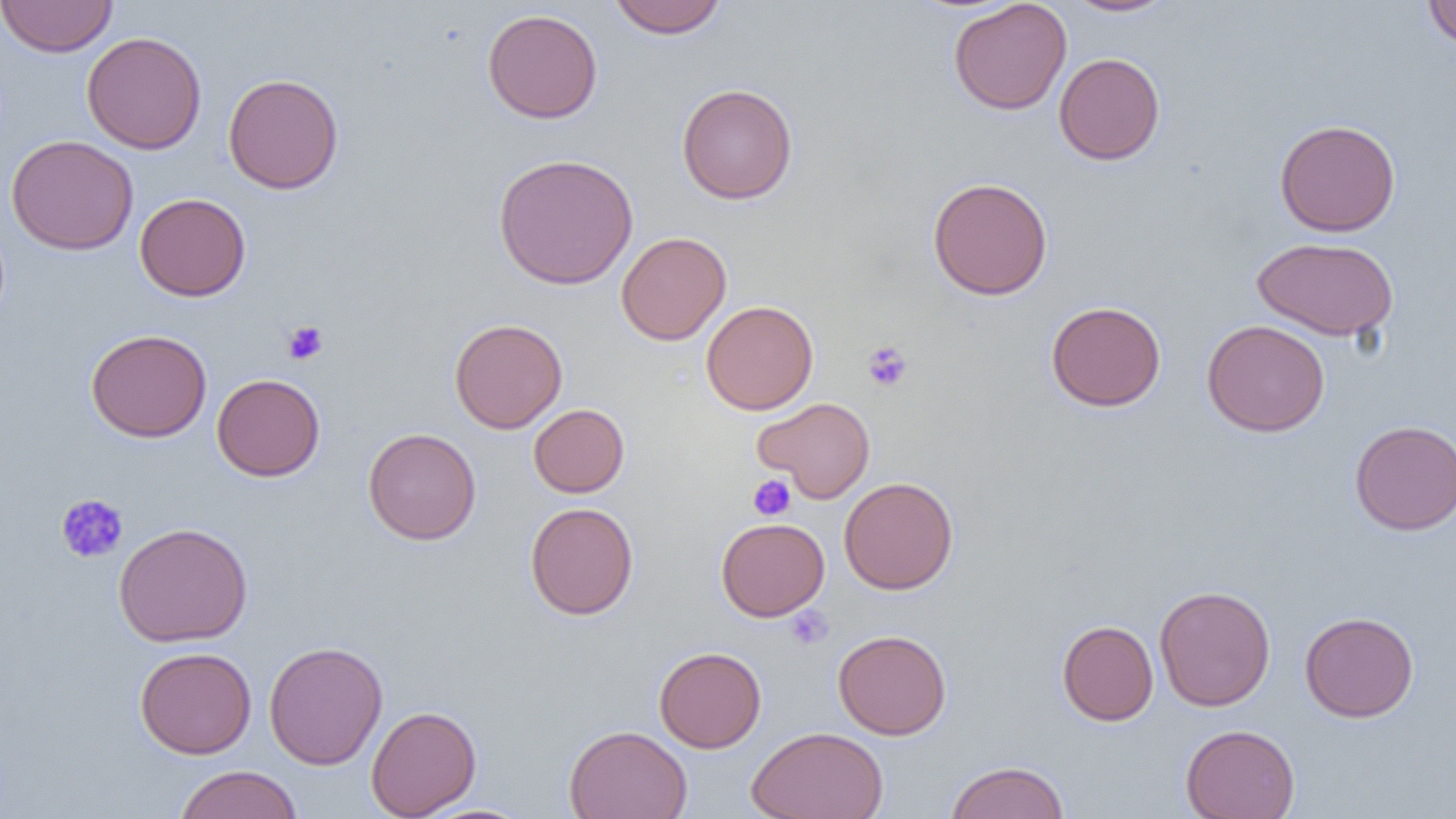
slide-level diagnosis = no evidence of blood parasites
modality = light microscopy
magnification = 1000x
uninfected red blood cell locations = approximate bounding boxes as (x1,y1)-(x2,y2) corner pairs in pixels: (0,0)-(118,57), (608,0)-(728,39), (948,0)-(1072,116), (1064,0)-(1177,17), (1423,1)-(1456,49), (482,8)-(603,124), (82,31)-(206,154), (1053,52)-(1165,165), (222,73)-(345,194), (676,83)-(798,205), (1274,119)-(1401,236), (6,134)-(138,255), (493,153)-(638,290), (927,177)-(1053,300), (135,192)-(251,301), (615,231)-(731,345), (1252,236)-(1398,341), (701,300)-(818,415), (1045,301)-(1166,412), (449,318)-(567,434), (1202,319)-(1330,437), (85,328)-(212,443), (212,373)-(325,481), (753,396)-(876,503), (528,404)-(629,497), (1349,420)-(1456,535), (363,427)-(481,545), (839,477)-(959,595), (524,501)-(638,620), (716,517)-(829,621), (113,521)-(253,647), (1154,585)-(1276,711), (1299,611)-(1419,722), (1057,620)-(1158,726), (833,629)-(951,740), (264,640)-(388,770), (134,646)-(257,759), (654,646)-(766,753), (366,705)-(482,818), (1180,724)-(1300,819), (564,725)-(692,819), (746,726)-(889,819), (945,760)-(1070,819), (173,765)-(303,819)
field of view = one of a larger specimen
preparation = thin blood smear
platelet locations = approximate bounding boxes as (x1,y1)-(x2,y2) corner pairs in pixels: (282,320)-(329,365), (863,341)-(913,392), (748,475)-(796,521), (56,494)-(128,564), (785,606)-(834,650)
image size = 1456×819 pixels